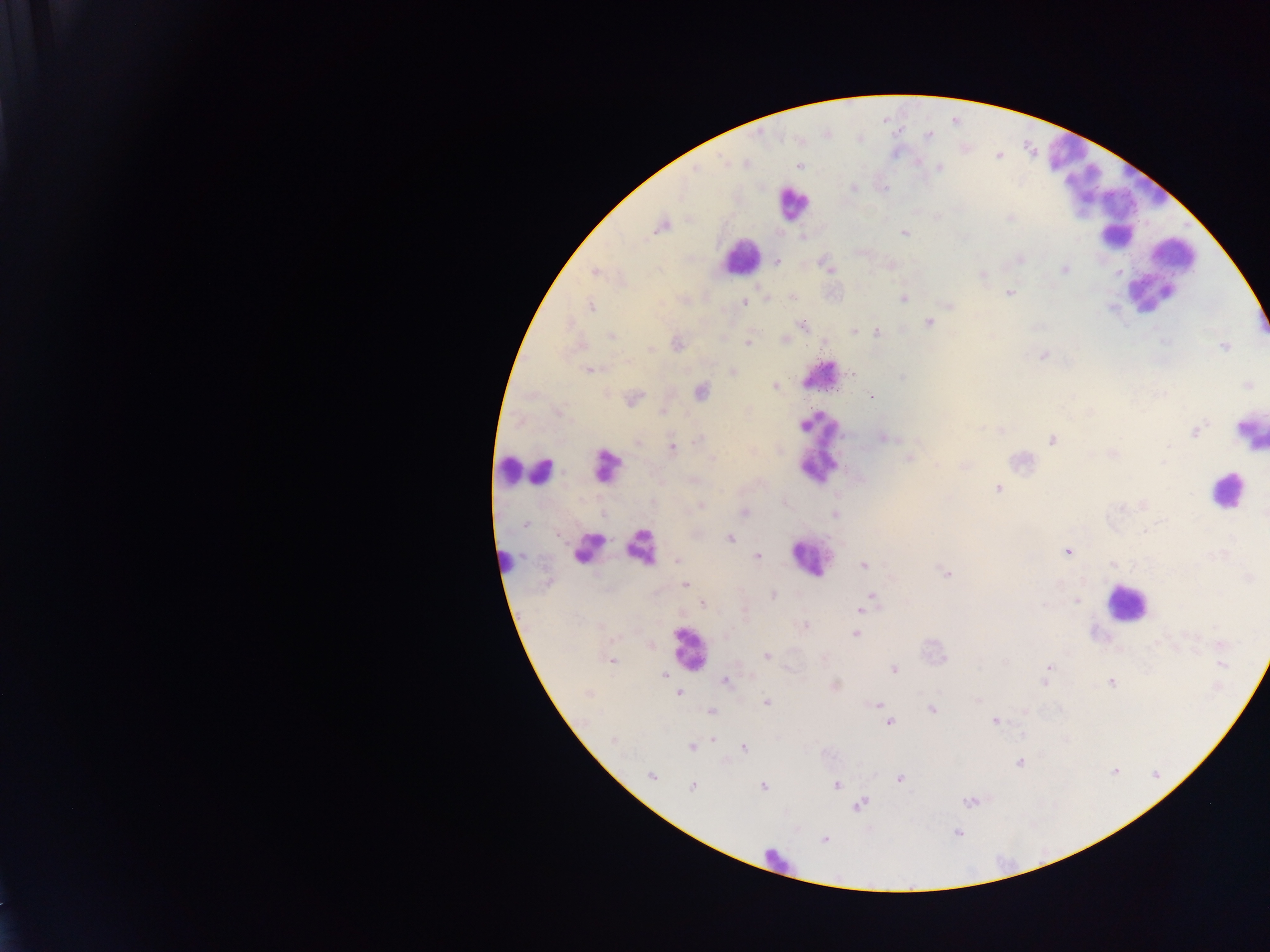 Approximate centers as x y in pixels. Malaria parasite locations: 929 134; 799 165; 939 167; 696 168; 854 188; 884 189; 1010 218; 662 226; 905 233; 802 237; 1020 258; 777 261; 829 267; 1064 270; 595 272; 1118 272; 982 276; 1009 293; 792 297; 767 298; 903 299; 744 303; 950 305; 590 306; 929 323; 802 326; 854 331; 877 332; 612 336; 783 339; 678 343; 748 343; 1225 347; 651 350; 1042 355; 589 370; 733 371; 851 373; 902 377; 1247 385; 775 386; 702 391; 872 397; 634 398; 663 412; 1197 431; 884 437; 1051 439; 698 440; 637 443; 672 446; 1169 447; 1113 453; 712 458; 908 459; 1164 462; 997 489; 701 505; 1121 507; 744 512; 835 515; 526 524; 730 539; 1067 551; 757 556; 677 560; 1113 563; 863 565; 946 573; 685 585; 773 595; 873 597; 1077 601; 868 602; 702 604; 861 609; 805 625; 856 634; 1221 644; 767 656; 612 661; 1222 664; 1049 667; 894 669; 664 675; 1047 675; 726 681; 1044 681; 1110 682; 835 686; 680 693; 588 694; 766 702; 876 705; 932 710; 710 711; 994 721; 888 722; 713 739; 613 740; 691 747; 744 748; 1020 763; 1114 771; 651 776; 900 778; 836 784; 692 786; 763 786; 969 802; 860 805; 957 832; 824 840. Leukocyte locations (subset; some below the resolvable size): 1063 150; 1148 181; 1080 184; 792 203; 1113 214; 1173 254; 739 256; 1148 294; 819 376; 1250 431; 817 442; 506 470; 606 470; 541 474; 1225 491; 590 545; 643 546; 812 557; 504 563; 1125 604; 687 647; 775 860. Photographed through a microscope with a mobile-phone camera. Thick blood film. Image is 1270×952 pixels. Collected in Ghana. One field of view.